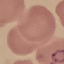
Summary:
  - Malaria status: parasitized
  - Image type: automatically extracted cell patch, resized to 64 × 64 pixels
  - Capture: smartphone camera at the microscope eyepiece
  - Stain: Giemsa
  - Preparation: thin smear